Assess the morphology of the erythrocytes.
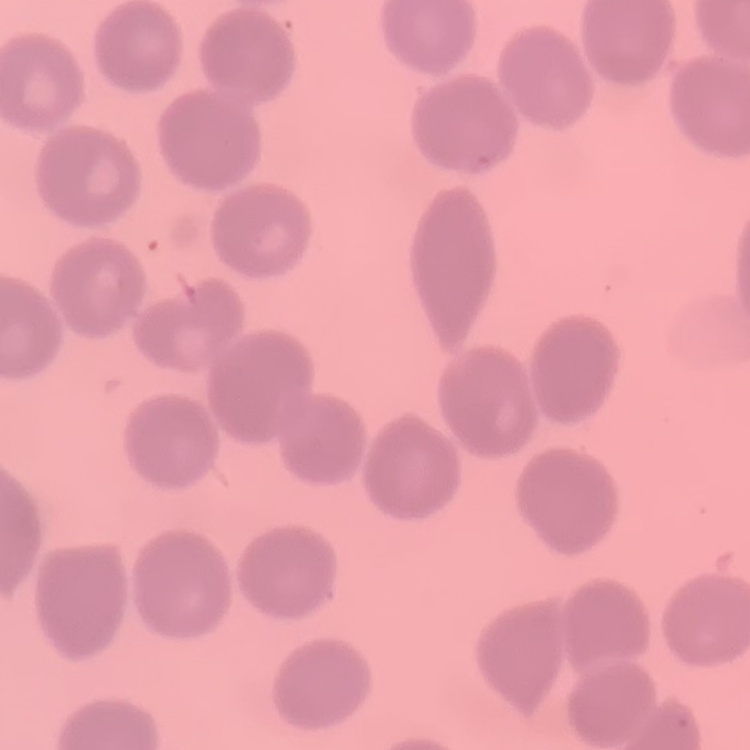

They show no rouleaux formation.

Summary:
  - Stain: Field's or Giemsa
  - Image type: one tile cut from a larger photomicrograph
  - Preparation: thin blood film